Report the malaria status of this cell.
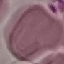
Uninfected.

Giemsa stain. Acquired by smartphone through the microscope eyepiece. Thin blood smear. Automatically extracted cell patch, resized to 64 × 64 pixels.